Assess this cell for malaria.
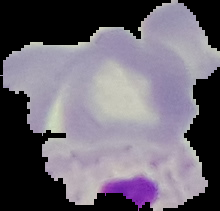

It is uninfected.

image size = 220×211 pixels
image type = segmented cell region with the area outside set to black
preparation = thin blood smear